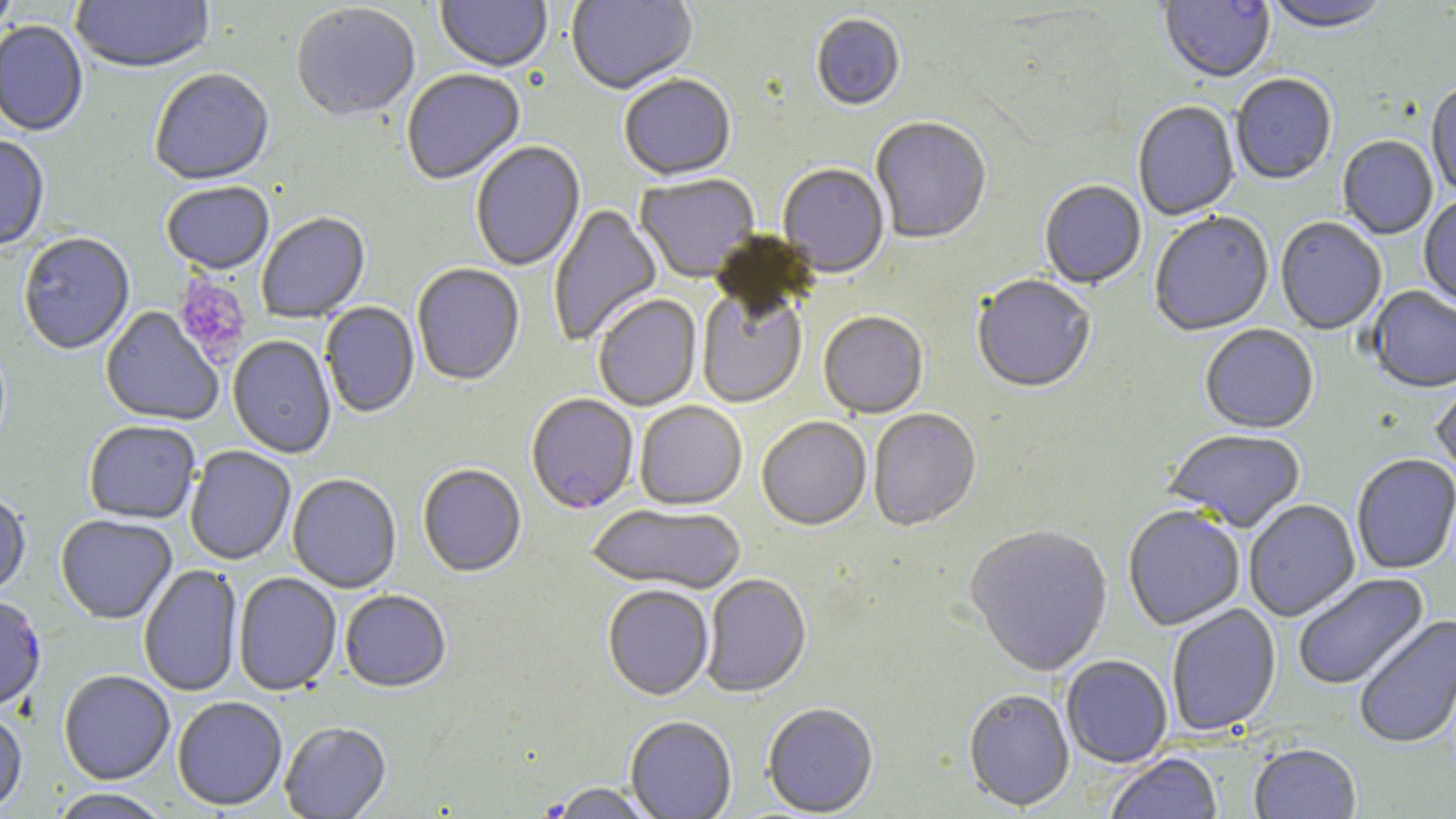

{
  "slide_level_diagnosis": "Plasmodium falciparum",
  "preparation": "thin blood film",
  "modality": "light microscopy",
  "uninfected_red_blood_cell_locations": "approximate bounding boxes as named x1/y1/x2/y2 corners in pixels: (x1=0, y1=0, x2=20, y2=40), (x1=70, y1=0, x2=215, y2=76), (x1=435, y1=0, x2=552, y2=74), (x1=566, y1=0, x2=698, y2=97), (x1=1158, y1=0, x2=1275, y2=85), (x1=1263, y1=1, x2=1392, y2=36), (x1=291, y1=5, x2=420, y2=125), (x1=811, y1=15, x2=906, y2=113), (x1=0, y1=22, x2=88, y2=138), (x1=149, y1=70, x2=275, y2=188), (x1=401, y1=70, x2=526, y2=187), (x1=1230, y1=75, x2=1337, y2=186), (x1=619, y1=76, x2=737, y2=182), (x1=1426, y1=83, x2=1456, y2=197), (x1=1133, y1=102, x2=1240, y2=221), (x1=870, y1=119, x2=992, y2=246), (x1=0, y1=137, x2=50, y2=253), (x1=1337, y1=137, x2=1437, y2=240), (x1=471, y1=142, x2=586, y2=273), (x1=777, y1=165, x2=889, y2=279), (x1=634, y1=175, x2=761, y2=285), (x1=1039, y1=182, x2=1146, y2=291), (x1=160, y1=183, x2=274, y2=276), (x1=1418, y1=197, x2=1456, y2=309), (x1=548, y1=204, x2=663, y2=348), (x1=257, y1=213, x2=371, y2=324), (x1=1149, y1=213, x2=1274, y2=338), (x1=1275, y1=218, x2=1387, y2=336), (x1=19, y1=234, x2=135, y2=356), (x1=411, y1=265, x2=525, y2=387), (x1=971, y1=277, x2=1096, y2=395), (x1=1366, y1=287, x2=1456, y2=395), (x1=696, y1=290, x2=809, y2=409), (x1=593, y1=295, x2=703, y2=412), (x1=320, y1=303, x2=419, y2=419), (x1=99, y1=307, x2=224, y2=427), (x1=818, y1=313, x2=929, y2=420), (x1=1200, y1=326, x2=1319, y2=435), (x1=228, y1=336, x2=336, y2=459), (x1=1431, y1=372, x2=1456, y2=481), (x1=634, y1=402, x2=747, y2=512), (x1=868, y1=410, x2=981, y2=533), (x1=757, y1=418, x2=871, y2=532), (x1=83, y1=421, x2=200, y2=525), (x1=1163, y1=431, x2=1306, y2=534), (x1=185, y1=447, x2=296, y2=566), (x1=1351, y1=455, x2=1456, y2=575), (x1=417, y1=465, x2=527, y2=579), (x1=287, y1=475, x2=402, y2=593), (x1=0, y1=493, x2=31, y2=600), (x1=1244, y1=500, x2=1360, y2=623), (x1=587, y1=504, x2=746, y2=595), (x1=1123, y1=507, x2=1245, y2=632), (x1=56, y1=515, x2=177, y2=625), (x1=964, y1=526, x2=1113, y2=679), (x1=139, y1=565, x2=243, y2=697), (x1=233, y1=573, x2=341, y2=697), (x1=1293, y1=573, x2=1430, y2=690), (x1=701, y1=574, x2=812, y2=699), (x1=603, y1=585, x2=714, y2=702), (x1=340, y1=591, x2=452, y2=694), (x1=0, y1=597, x2=46, y2=714), (x1=1166, y1=605, x2=1281, y2=737), (x1=1353, y1=614, x2=1455, y2=750), (x1=1061, y1=656, x2=1173, y2=769), (x1=58, y1=671, x2=175, y2=785), (x1=963, y1=691, x2=1075, y2=812), (x1=172, y1=696, x2=288, y2=812), (x1=763, y1=704, x2=879, y2=817), (x1=0, y1=711, x2=27, y2=816), (x1=625, y1=717, x2=737, y2=819), (x1=280, y1=722, x2=392, y2=819), (x1=1249, y1=745, x2=1361, y2=819), (x1=1104, y1=754, x2=1223, y2=819), (x1=547, y1=783, x2=659, y2=818), (x1=50, y1=788, x2=170, y2=819)",
  "image_size": "1456×819 pixels",
  "field_of_view": "single",
  "plasmodium_falciparum_infected_red_blood_cell_locations": "approximate bounding boxes as named x1/y1/x2/y2 corners in pixels: (x1=525, y1=395, x2=638, y2=515)",
  "magnification": "1000x",
  "stain": "May-Grünwald-Giemsa",
  "platelet_locations": "approximate bounding boxes as named x1/y1/x2/y2 corners in pixels: (x1=173, y1=275, x2=251, y2=365)"
}